Assess this cell for malaria.
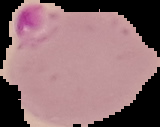
Parasitized.

The area outside the segmented cell region is set to black. From a thin blood smear. Image is 160×127 pixels.